Report the malaria status of this cell.
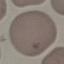
It is uninfected.

Giemsa-stained preparation. Cell patch, automatically extracted from a larger field of view and resized to 64 × 64 pixels. Thin smear of blood. Acquired by smartphone through the microscope eyepiece.